Locate every Plasmodium parasite.
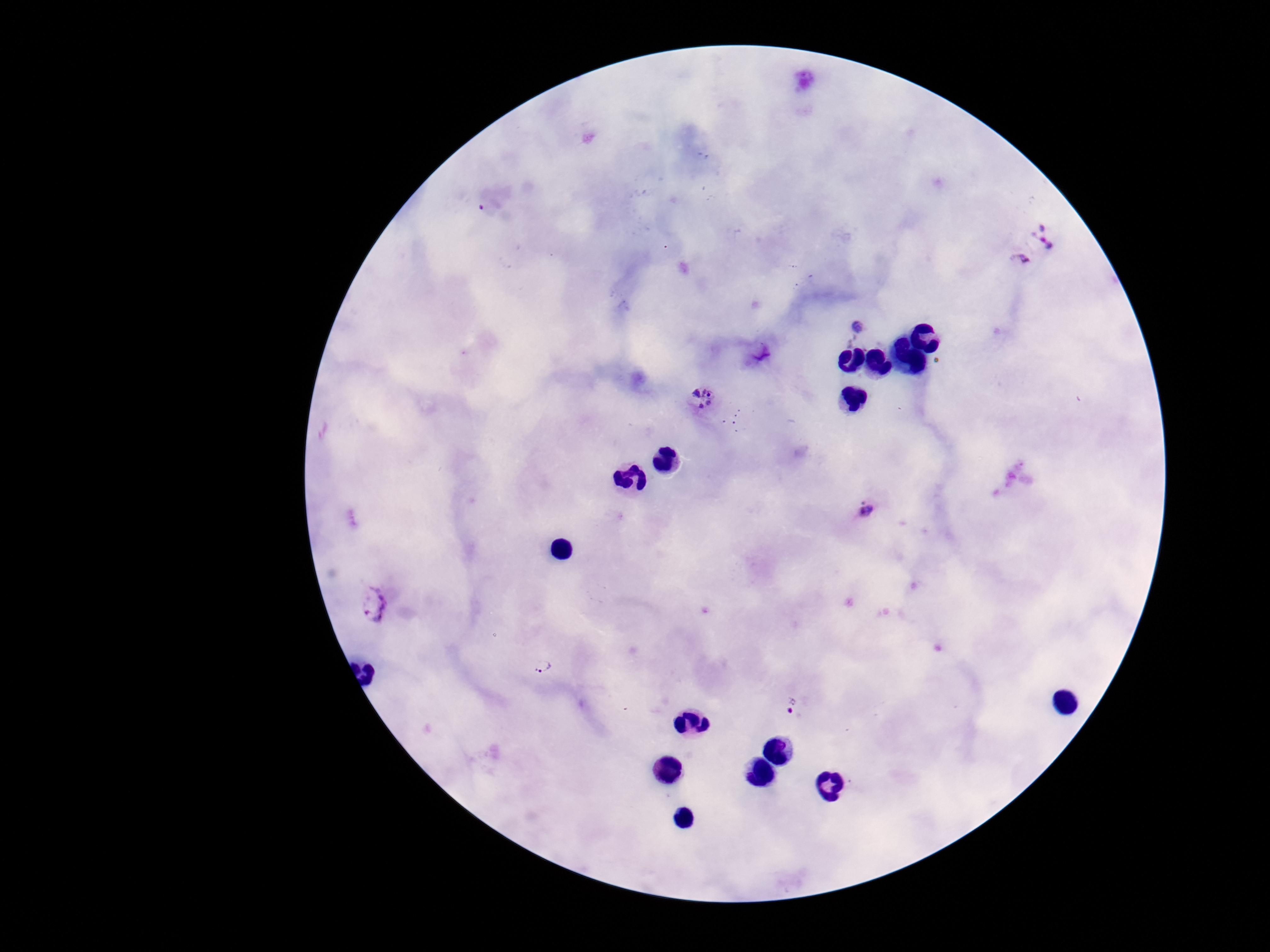
Approximate centers as (x, y) in pixels.
Plasmodium parasites: (1049, 234), (1013, 266), (860, 325), (759, 350), (701, 400), (866, 510), (372, 606), (542, 663), (793, 709).

field of view = single
image size = 1270×952 pixels
magnification = 100x
patient malaria status = positive
capture = smartphone camera through the microscope eyepiece
stain = Giemsa
preparation = thick blood film